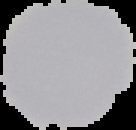

The area outside the segmented cell region is set to black. Result: negative for Plasmodium parasites. From a thin blood film. Image is 136×130 pixels.